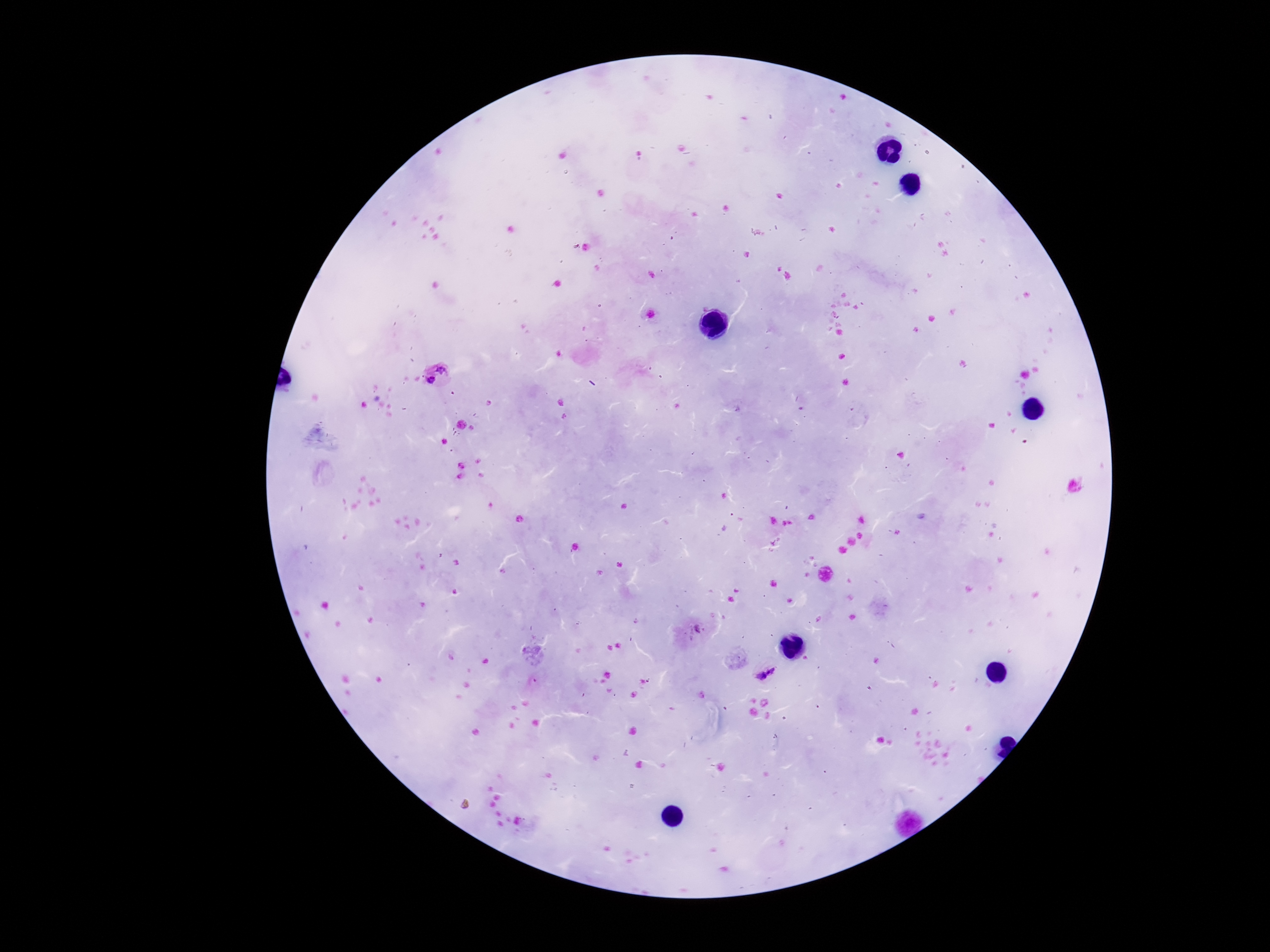
Approximate centers as {x, y} in pixels. Plasmodium parasite locations: {442, 369}, {430, 382}, {698, 628}, {766, 674}. Patient malaria status: infected. 100x magnification. One field from this slide. Giemsa-stained preparation. Image is 1270×952 pixels. Smartphone photograph taken through the microscope eyepiece. Thick blood film.